Outline platelets.
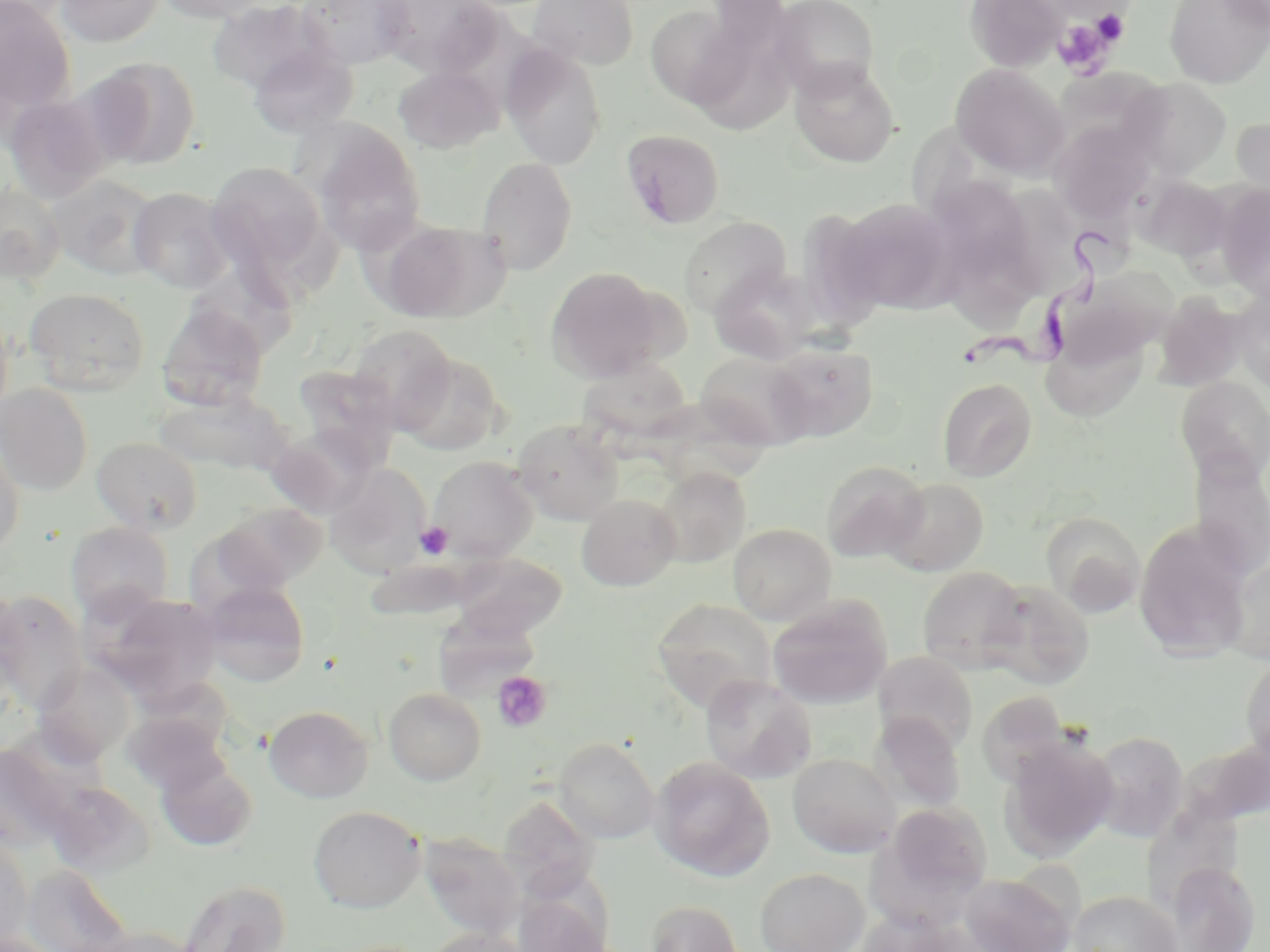

Approximate bounding boxes as [x1, y1, x2, y2] in pixels.
Platelets: [1089, 7, 1131, 46], [1051, 18, 1116, 74], [415, 521, 453, 560], [492, 671, 553, 733].

Trypanosoma brucei locations = approximate bounding boxes as [x1, y1, x2, y2] in pixels: [962, 230, 1116, 381]
slide-level diagnosis = Trypanosoma brucei
preparation = thin blood smear
uninfected red blood cell locations = approximate bounding boxes as [x1, y1, x2, y2] in pixels: [0, 0, 76, 113], [54, 0, 166, 47], [151, 0, 277, 23], [294, 0, 414, 70], [376, 0, 499, 76], [527, 0, 639, 70], [770, 0, 880, 97], [964, 0, 1066, 72], [1165, 0, 1269, 88], [1217, 0, 1270, 31], [207, 1, 330, 93], [645, 4, 746, 109], [693, 24, 802, 132], [248, 42, 359, 139], [500, 46, 608, 170], [84, 57, 200, 170], [790, 61, 900, 168], [951, 63, 1070, 180], [393, 65, 503, 154], [1051, 68, 1171, 163], [1124, 77, 1232, 179], [2, 94, 111, 203], [1231, 116, 1270, 211], [908, 118, 1022, 212], [306, 122, 428, 255], [1049, 122, 1156, 222], [620, 129, 725, 229], [477, 157, 578, 275], [207, 161, 327, 276], [46, 173, 162, 279], [1134, 174, 1232, 262], [1214, 183, 1270, 300], [996, 184, 1082, 295], [0, 185, 66, 284], [128, 187, 235, 293], [836, 197, 960, 314], [679, 216, 791, 317], [377, 218, 508, 323], [951, 252, 1034, 335], [710, 265, 819, 365], [1052, 265, 1177, 370], [544, 266, 666, 383], [192, 272, 302, 358], [25, 287, 150, 394], [1230, 288, 1270, 391], [1152, 292, 1250, 391], [157, 300, 269, 411], [0, 310, 14, 422], [346, 324, 457, 430], [1041, 331, 1150, 423], [764, 342, 878, 442], [397, 352, 506, 456], [694, 352, 810, 451], [576, 356, 693, 440], [293, 364, 402, 465], [1176, 375, 1270, 484], [938, 377, 1036, 481], [0, 383, 93, 496], [154, 388, 290, 476], [513, 419, 624, 525], [267, 426, 379, 518], [92, 436, 202, 534], [0, 439, 25, 559], [1189, 451, 1270, 581], [427, 455, 539, 562], [822, 460, 929, 562], [324, 462, 431, 577], [652, 466, 751, 568], [883, 477, 989, 576], [576, 494, 681, 591], [214, 501, 328, 592], [1042, 513, 1145, 616], [1133, 520, 1253, 663], [66, 521, 173, 621], [728, 523, 836, 625], [449, 552, 567, 640], [366, 556, 523, 614], [1223, 559, 1270, 665], [917, 566, 1028, 673], [983, 579, 1094, 689], [200, 580, 310, 687], [0, 586, 22, 692], [0, 591, 87, 709], [94, 591, 225, 700], [767, 596, 893, 710], [651, 598, 777, 713], [432, 608, 542, 698], [874, 652, 977, 753], [1240, 653, 1270, 766], [33, 662, 138, 765], [700, 674, 817, 784], [383, 687, 486, 785], [976, 690, 1072, 788], [264, 705, 373, 803], [123, 710, 231, 797], [871, 712, 966, 814], [1087, 731, 1189, 843], [1000, 734, 1118, 861], [553, 737, 660, 843], [787, 752, 900, 858], [649, 755, 775, 882], [157, 758, 259, 852], [47, 782, 155, 877], [498, 795, 599, 900], [873, 800, 995, 919], [1141, 800, 1246, 913], [309, 805, 426, 913], [418, 832, 526, 940], [0, 836, 34, 945], [1166, 862, 1261, 952], [22, 864, 133, 952], [755, 867, 869, 952], [961, 871, 1077, 952], [177, 878, 292, 952], [511, 890, 613, 952], [1069, 890, 1183, 951], [645, 899, 744, 952], [853, 910, 972, 952], [89, 926, 202, 952], [423, 928, 533, 952], [0, 930, 66, 952]
magnification = 1000x
image size = 1270×952 pixels
field of view = single
modality = optical microscopy
stain = May-Grünwald-Giemsa